State which parasite is depicted.
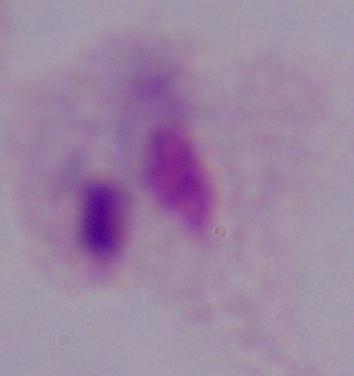

A trichomonad.

1000x magnification. Micrograph.